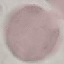

{
  "malaria_status": "uninfected",
  "image_type": "cell patch, automatically extracted from a larger field of view and resized to 64 × 64 pixels",
  "stain": "Giemsa",
  "capture": "smartphone through the microscope eyepiece",
  "preparation": "thin blood film"
}